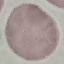

Summary:
  - Malaria status: uninfected
  - Stain: Giemsa
  - Preparation: thin blood smear
  - Capture: smartphone through the microscope eyepiece
  - Image type: cell patch, automatically extracted from a larger field of view and resized to 64 × 64 pixels